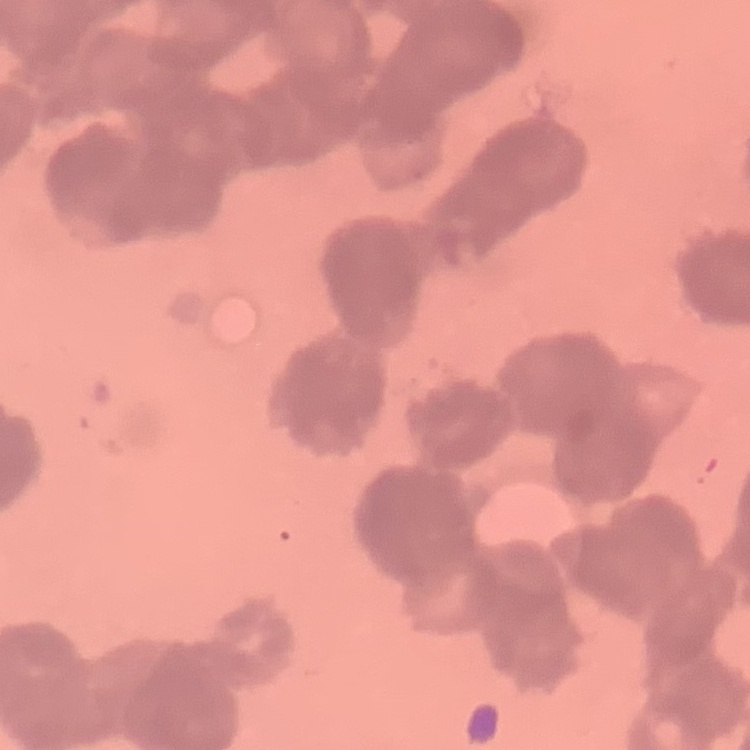

red blood cell morphology = rouleaux formation
image type = one tile cut from a larger photomicrograph
stain = Field's or Giemsa
preparation = thin blood smear